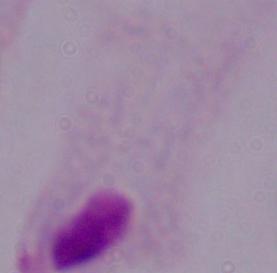
magnification = 1000x
identification = trichomonad
modality = photomicrograph